Point out each leukocyte.
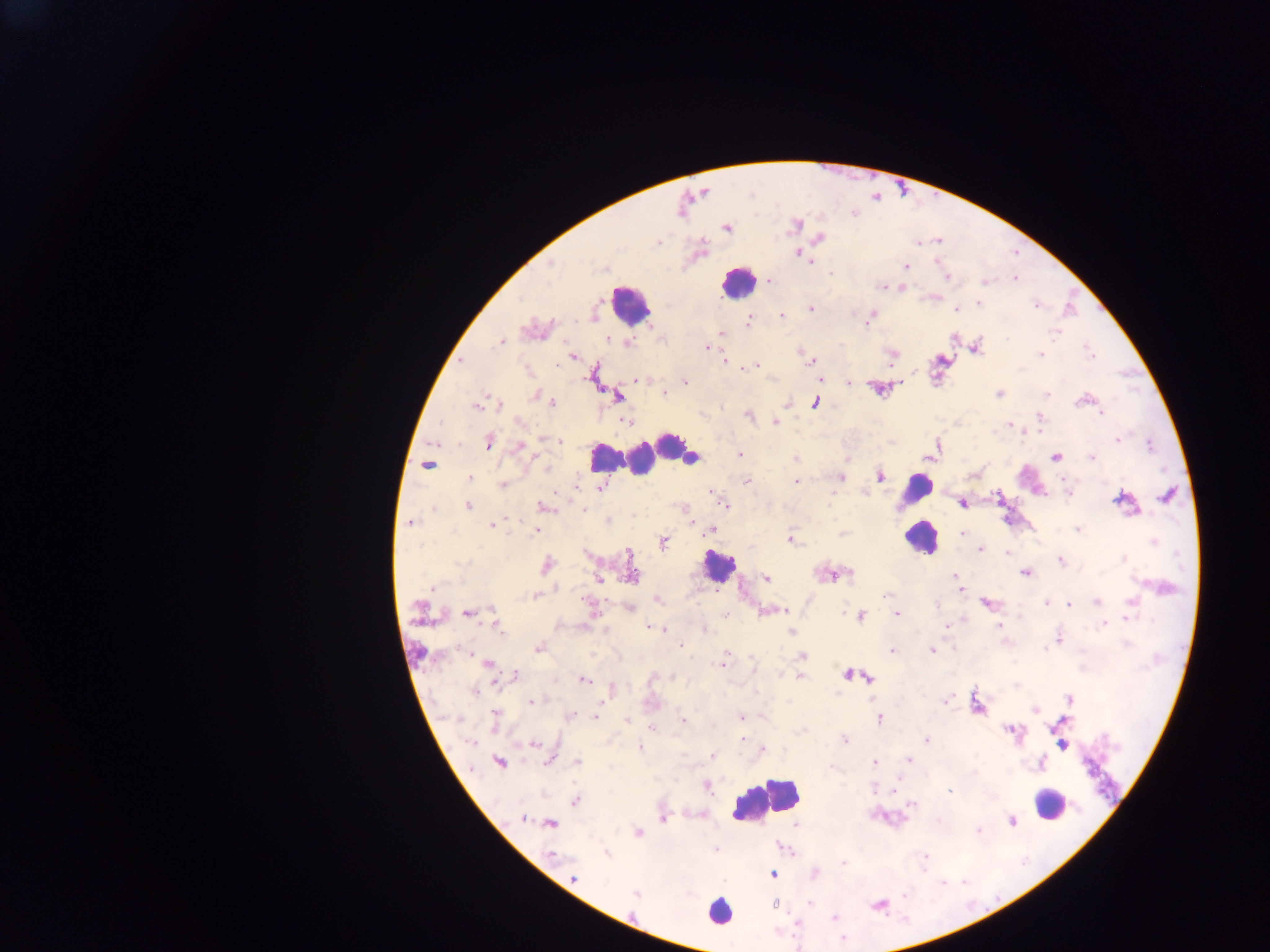
Approximate centers as [x, y] in pixels.
Leukocytes: [739, 282], [629, 305], [671, 447], [649, 454], [625, 456], [689, 457], [605, 458], [917, 488], [922, 536], [718, 566], [766, 797], [1050, 803], [718, 911].

preparation = thick blood film
field of view = single
image size = 1270×952 pixels
capture = mobile-phone photograph through a microscope
Plasmodium parasite locations = approximate centers as [x, y] in pixels: [727, 227], [819, 238], [658, 241], [917, 242], [798, 252], [810, 261], [905, 266], [947, 276], [1014, 277], [768, 281], [883, 287], [901, 287], [934, 297], [979, 304], [1037, 304], [810, 309], [956, 309], [782, 315], [870, 317], [748, 320], [534, 329], [1056, 331], [722, 332], [501, 341], [706, 347], [974, 347], [891, 354], [1040, 354], [572, 357], [725, 361], [810, 361], [755, 365], [744, 366], [820, 378], [636, 379], [684, 382], [848, 382], [879, 387], [998, 393], [663, 394], [1046, 394], [536, 395], [617, 396], [1085, 399], [552, 401], [815, 401], [478, 403], [497, 403], [787, 403], [749, 415], [626, 421], [774, 422], [1010, 425], [559, 439], [1116, 439], [488, 442], [519, 447], [930, 454], [740, 455], [1091, 456], [795, 457], [1055, 457], [847, 459], [427, 465], [880, 475], [840, 477], [470, 479], [746, 480], [796, 481], [1064, 481], [503, 484], [576, 485], [599, 487], [711, 492], [1168, 494], [715, 495], [998, 497], [1123, 498], [961, 503], [723, 504], [468, 506], [543, 507], [584, 510], [606, 520], [409, 523], [492, 525], [536, 529], [710, 529], [1077, 529], [964, 534], [790, 538], [663, 541], [979, 550], [1060, 560], [546, 566], [1024, 572], [631, 573], [833, 574], [956, 574], [766, 578], [599, 580], [961, 589], [536, 596], [656, 600], [1097, 601], [987, 603], [1046, 603], [1069, 604], [630, 608], [420, 609], [774, 610], [782, 610], [468, 612], [895, 613], [726, 614], [860, 616], [1127, 616], [496, 623], [1103, 623], [998, 625], [649, 626], [946, 627], [660, 629], [703, 629], [790, 632], [1059, 639], [680, 645], [538, 647], [893, 650], [931, 650], [802, 656], [723, 664], [488, 665], [848, 674], [514, 676], [798, 676], [868, 677], [582, 680], [611, 688], [474, 691], [945, 699], [1069, 699], [531, 701], [976, 704], [1035, 710], [569, 716], [595, 716], [741, 717], [879, 718], [495, 720], [628, 720], [682, 720], [651, 727], [1010, 728], [741, 739], [926, 739], [844, 740], [535, 743], [1061, 743], [639, 748], [762, 750], [712, 756], [549, 759], [908, 759], [499, 762], [576, 762], [875, 763], [1041, 763], [706, 785], [949, 789], [575, 800], [910, 804], [523, 819], [662, 819], [1010, 820], [550, 823], [979, 830], [637, 832], [716, 850], [606, 853], [551, 856], [925, 856], [844, 863], [773, 874], [574, 879], [636, 892], [774, 905]
country = Ghana